Identify the parasite.
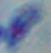
This is Toxoplasma gondii.

magnification = 1000x
modality = photomicrograph